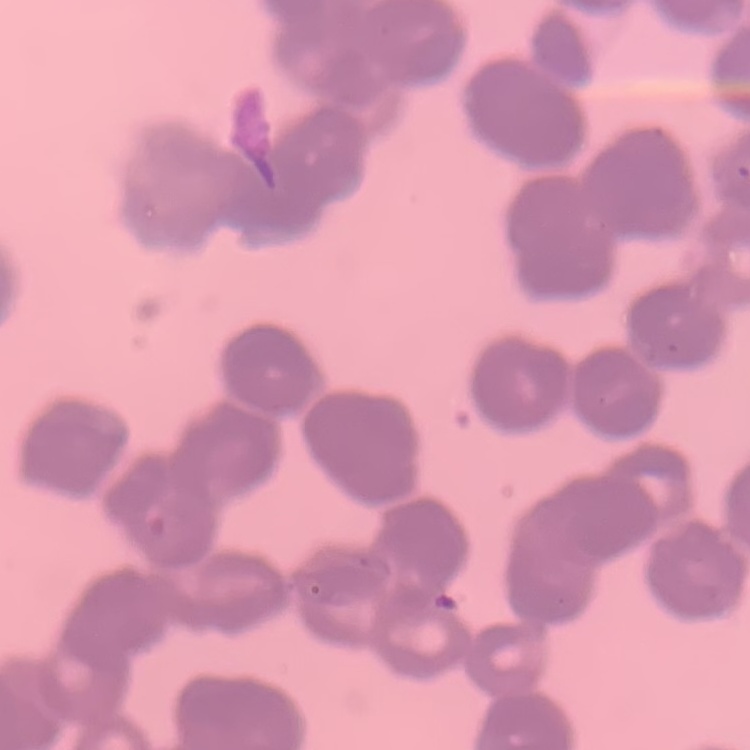

Summary:
  - Erythrocyte morphology: rouleaux formation
  - Stain: Field's or Giemsa
  - Image type: one tile cut from a larger photomicrograph
  - Preparation: thin blood smear